Assess the morphology of the erythrocytes.
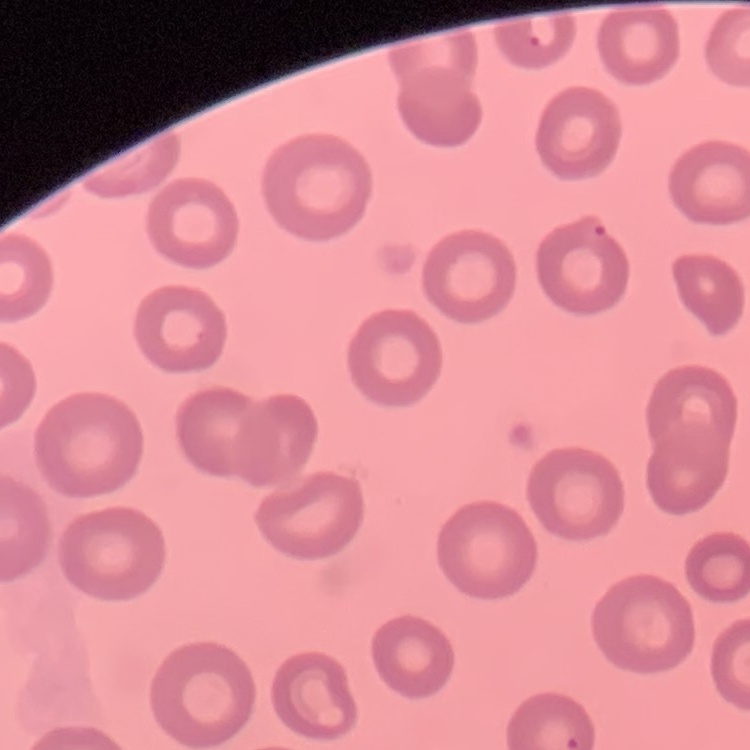
No rouleaux formation.

Thin blood smear. Square crop of a larger photomicrograph. Stained with either Field's or Giemsa.